Name the parasite shown.
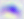
This is Toxoplasma gondii.

Photomicrograph. 400x magnification.